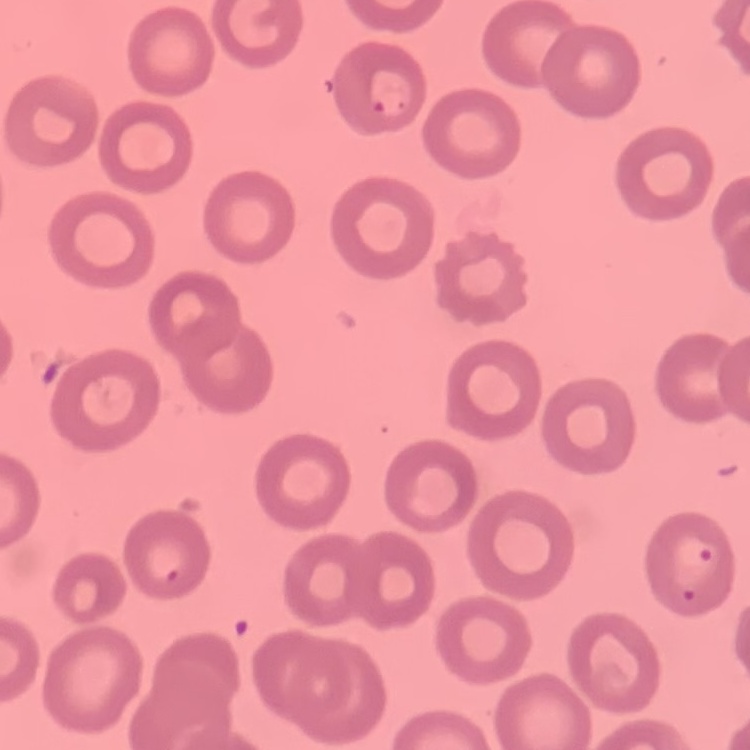

Summary:
  - Erythrocyte morphology: no rouleaux formation
  - Preparation: thin peripheral smear
  - Stain: Field's or Giemsa
  - Image type: one tile cut from a larger photomicrograph